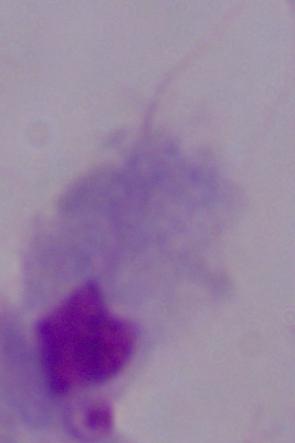 Micrograph. A trichomonad is shown. 1000x magnification.